Identify the parasite.
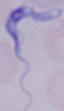

A trypanosome.

Micrograph. 1000x magnification.